Name the parasite shown.
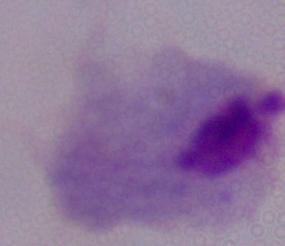

A trichomonad.

Micrograph. Captured at 1000x magnification.